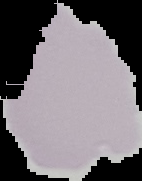

Summary:
  - Preparation: thin blood film
  - Image size: 142×181 pixels
  - Malaria status: uninfected
  - Image type: segmented cell region on a black background